Name the blood parasite species.
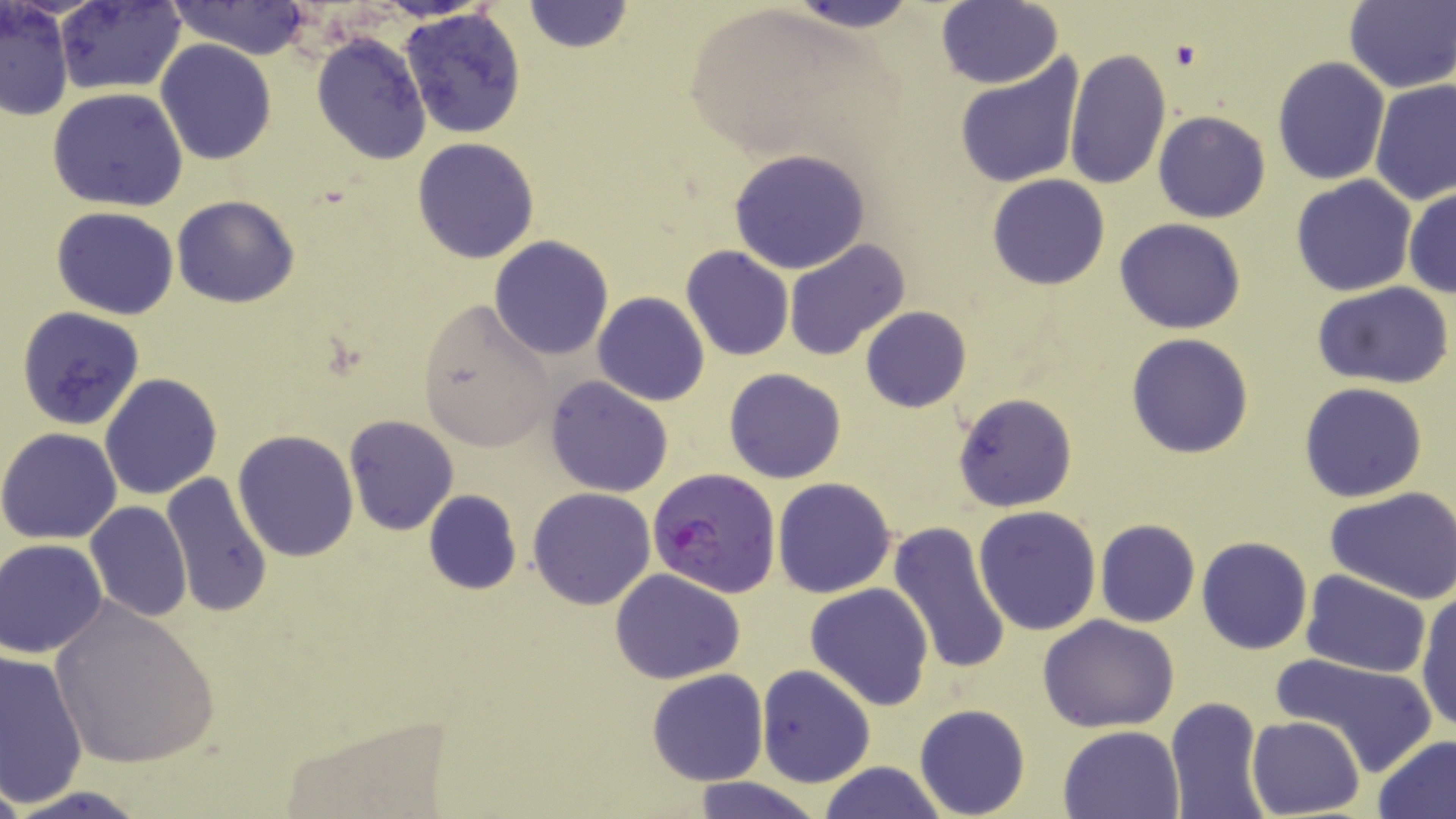
Plasmodium falciparum.

Approximate bounding boxes as named x1/y1/x2/y2 corners in pixels. Uninfected red blood cell locations: (x1=56, y1=0, x2=185, y2=95), (x1=783, y1=0, x2=921, y2=32), (x1=523, y1=1, x2=633, y2=54), (x1=1344, y1=1, x2=1456, y2=92), (x1=1, y1=2, x2=74, y2=122), (x1=166, y1=2, x2=314, y2=56), (x1=935, y1=2, x2=1063, y2=88), (x1=399, y1=7, x2=530, y2=140), (x1=310, y1=32, x2=432, y2=164), (x1=154, y1=40, x2=277, y2=165), (x1=1064, y1=49, x2=1170, y2=192), (x1=954, y1=54, x2=1086, y2=189), (x1=1272, y1=56, x2=1390, y2=185), (x1=1369, y1=79, x2=1455, y2=204), (x1=48, y1=87, x2=187, y2=210), (x1=1143, y1=106, x2=1261, y2=330), (x1=1153, y1=110, x2=1270, y2=222), (x1=412, y1=136, x2=541, y2=264), (x1=728, y1=149, x2=870, y2=275), (x1=988, y1=174, x2=1110, y2=290), (x1=1290, y1=176, x2=1417, y2=296), (x1=1404, y1=187, x2=1455, y2=299), (x1=173, y1=195, x2=300, y2=307), (x1=52, y1=207, x2=179, y2=320), (x1=1116, y1=219, x2=1245, y2=334), (x1=489, y1=236, x2=615, y2=359), (x1=785, y1=237, x2=911, y2=361), (x1=680, y1=247, x2=796, y2=363), (x1=1312, y1=280, x2=1453, y2=389), (x1=592, y1=292, x2=709, y2=406), (x1=416, y1=298, x2=558, y2=449), (x1=15, y1=306, x2=146, y2=430), (x1=860, y1=307, x2=971, y2=412), (x1=1126, y1=333, x2=1254, y2=458), (x1=724, y1=367, x2=846, y2=484), (x1=100, y1=372, x2=221, y2=500), (x1=545, y1=376, x2=673, y2=497), (x1=1299, y1=382, x2=1428, y2=502), (x1=952, y1=392, x2=1076, y2=512), (x1=343, y1=414, x2=459, y2=536), (x1=0, y1=427, x2=123, y2=546), (x1=232, y1=429, x2=360, y2=561), (x1=160, y1=473, x2=275, y2=618), (x1=771, y1=477, x2=896, y2=597), (x1=1325, y1=486, x2=1456, y2=603), (x1=527, y1=488, x2=655, y2=609), (x1=423, y1=489, x2=521, y2=595), (x1=85, y1=501, x2=192, y2=621), (x1=973, y1=504, x2=1103, y2=635), (x1=1095, y1=519, x2=1200, y2=628), (x1=886, y1=521, x2=1013, y2=676), (x1=1197, y1=536, x2=1312, y2=654), (x1=2, y1=538, x2=110, y2=657), (x1=610, y1=568, x2=745, y2=684), (x1=1300, y1=568, x2=1433, y2=677), (x1=805, y1=583, x2=934, y2=710), (x1=1414, y1=587, x2=1456, y2=735), (x1=45, y1=596, x2=224, y2=771), (x1=1040, y1=615, x2=1180, y2=733), (x1=0, y1=649, x2=90, y2=804), (x1=1275, y1=649, x2=1439, y2=775), (x1=756, y1=665, x2=874, y2=787), (x1=647, y1=669, x2=767, y2=785), (x1=1165, y1=696, x2=1270, y2=819), (x1=914, y1=703, x2=1030, y2=818), (x1=1245, y1=716, x2=1365, y2=818), (x1=1058, y1=724, x2=1185, y2=818), (x1=1373, y1=733, x2=1456, y2=819), (x1=818, y1=760, x2=947, y2=819), (x1=0, y1=775, x2=26, y2=819), (x1=687, y1=776, x2=822, y2=819), (x1=5, y1=785, x2=152, y2=819). Platelet locations: (x1=1171, y1=41, x2=1204, y2=71). Plasmodium falciparum-infected red blood cell locations: (x1=647, y1=467, x2=781, y2=597). Light microscopy. Single field of view. Image is 1456×819 pixels. Thin blood smear. May-Grünwald-Giemsa-stained preparation. 1000x magnification.